State the blood parasite species.
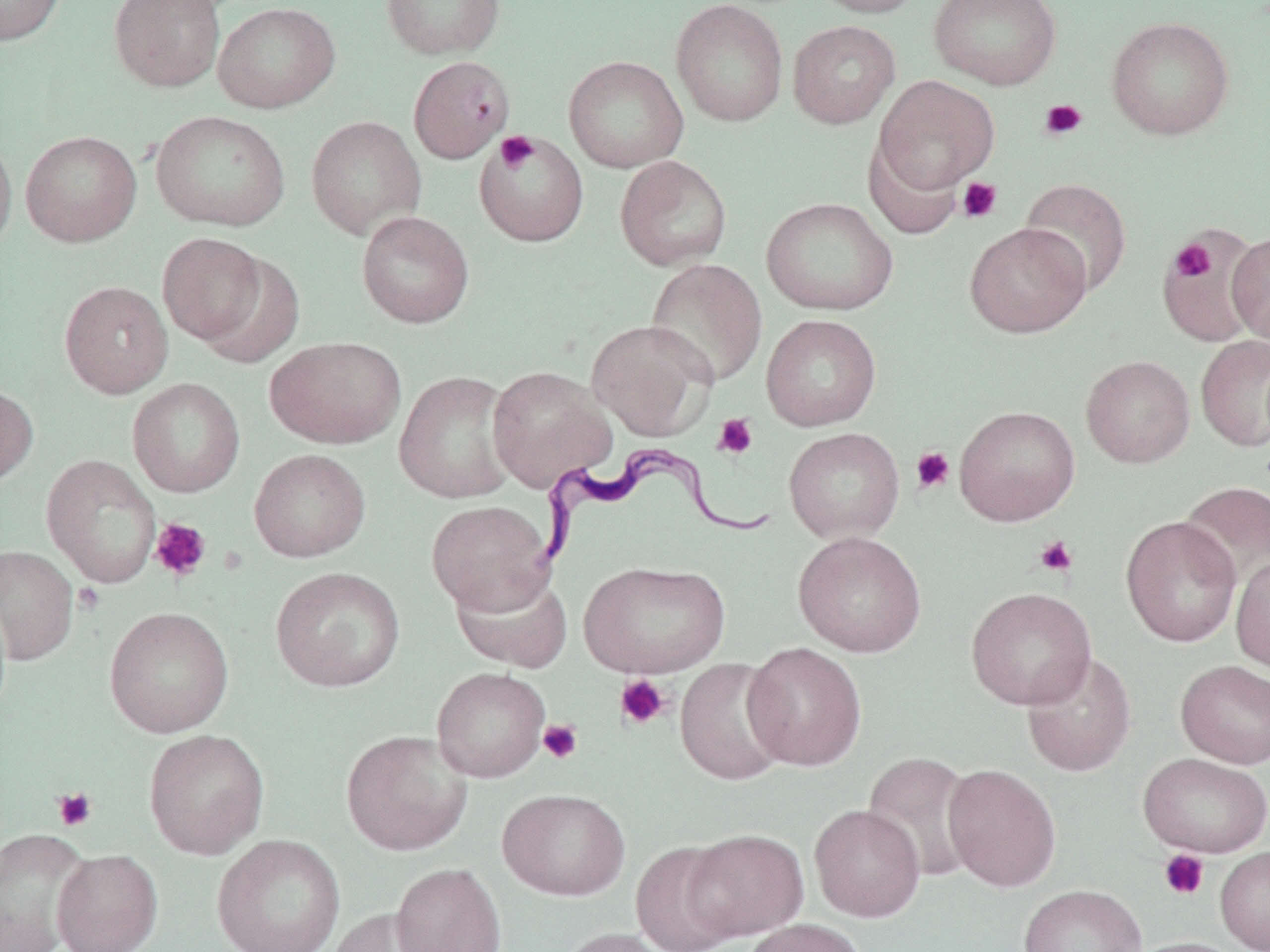
Trypanosoma brucei.

{
  "uninfected_red_blood_cell_locations": "approximate bounding boxes as (x1,y1)-(x2,y2) corner pairs in pixels: (0,0)-(66,45), (108,0)-(226,92), (381,0)-(505,60), (671,0)-(788,127), (807,0)-(927,18), (929,0)-(1062,90), (213,2)-(341,113), (1106,16)-(1235,141), (787,19)-(900,129), (407,55)-(515,163), (563,55)-(688,173), (872,75)-(1000,196), (150,110)-(290,231), (305,115)-(426,239), (20,130)-(142,247), (474,131)-(589,247), (0,132)-(17,257), (863,134)-(963,239), (614,156)-(732,270), (1018,177)-(1132,297), (761,197)-(899,316), (356,211)-(474,328), (964,222)-(1092,338), (1157,228)-(1265,347), (1227,231)-(1270,345), (157,233)-(266,345), (195,252)-(304,369), (645,258)-(767,387), (59,281)-(174,398), (760,314)-(881,431), (586,319)-(717,441), (1195,334)-(1270,452), (265,336)-(407,449), (1081,354)-(1195,468), (487,365)-(616,492), (394,370)-(518,503), (127,378)-(246,497), (0,383)-(38,487), (954,405)-(1080,526), (783,427)-(905,544), (249,449)-(370,561), (41,454)-(161,588), (1177,481)-(1270,595), (426,500)-(555,616), (1120,515)-(1242,648), (793,530)-(927,658), (0,545)-(79,666), (1231,553)-(1270,675), (579,560)-(730,678), (270,567)-(404,692), (450,569)-(573,673), (965,586)-(1096,710), (104,606)-(234,738), (742,642)-(867,771), (1021,652)-(1137,777), (674,658)-(791,785), (1175,660)-(1270,768), (431,666)-(550,782), (143,728)-(269,859), (341,729)-(473,856), (860,751)-(980,881), (1137,752)-(1270,858), (943,764)-(1061,891), (497,788)-(630,900), (809,804)-(925,921), (0,828)-(94,952), (682,828)-(809,941), (211,834)-(345,952), (631,841)-(743,952), (1215,845)-(1270,952), (52,849)-(163,952), (391,862)-(507,952), (1019,884)-(1146,952), (327,907)-(443,952), (741,918)-(867,952), (556,926)-(677,952), (1125,936)-(1251,952)",
  "stain": "May-Grünwald-Giemsa",
  "platelet_locations": "approximate bounding boxes as (x1,y1)-(x2,y2) corner pairs in pixels: (1039,98)-(1087,140), (496,131)-(538,171), (957,177)-(1001,223), (1164,234)-(1231,305), (1170,238)-(1216,284), (712,413)-(758,459), (911,447)-(955,494), (149,518)-(211,582), (1034,535)-(1078,577), (73,583)-(104,615), (615,674)-(672,730), (538,719)-(583,764), (53,788)-(97,831), (1158,849)-(1209,900)",
  "magnification": "1000x",
  "preparation": "thin blood smear",
  "modality": "optical microscopy",
  "trypanosoma_brucei_locations": "approximate bounding boxes as (x1,y1)-(x2,y2) corner pairs in pixels: (525,448)-(774,569)",
  "image_size": "1270×952 pixels",
  "field_of_view": "one of a larger specimen"
}